Classify this cell by malaria status.
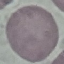
Uninfected.

Cell patch, automatically extracted from a larger field of view and resized to 64 × 64 pixels. Acquired by smartphone through the microscope eyepiece. Thin blood smear. Giemsa-stained preparation.